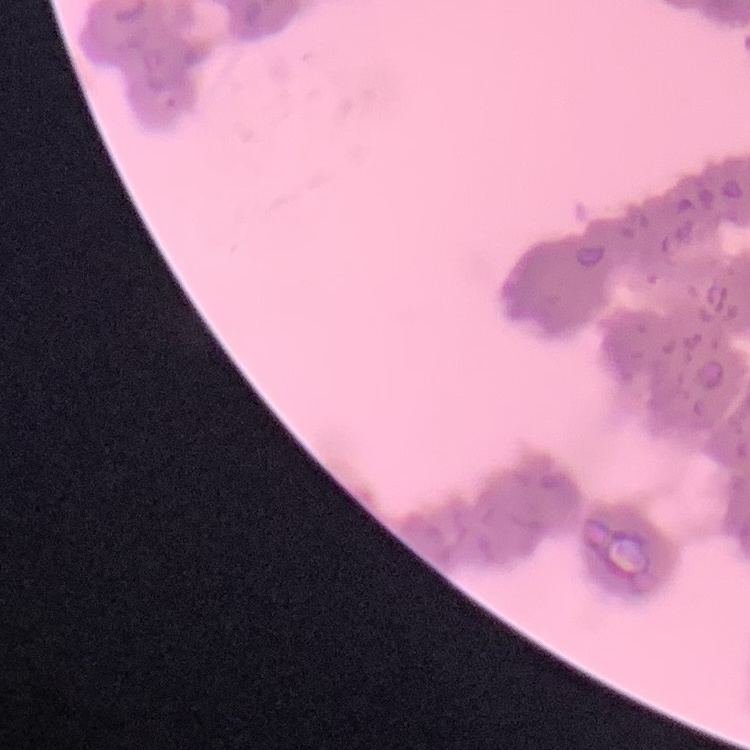 The erythrocytes exhibit rouleaux formation. Stained with either Field's or Giemsa. Thin blood film. Square crop of a larger photomicrograph.